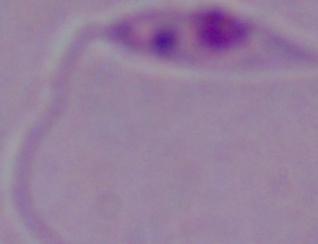 A Leishmania parasite is seen. Micrograph. Captured at 1000x magnification.